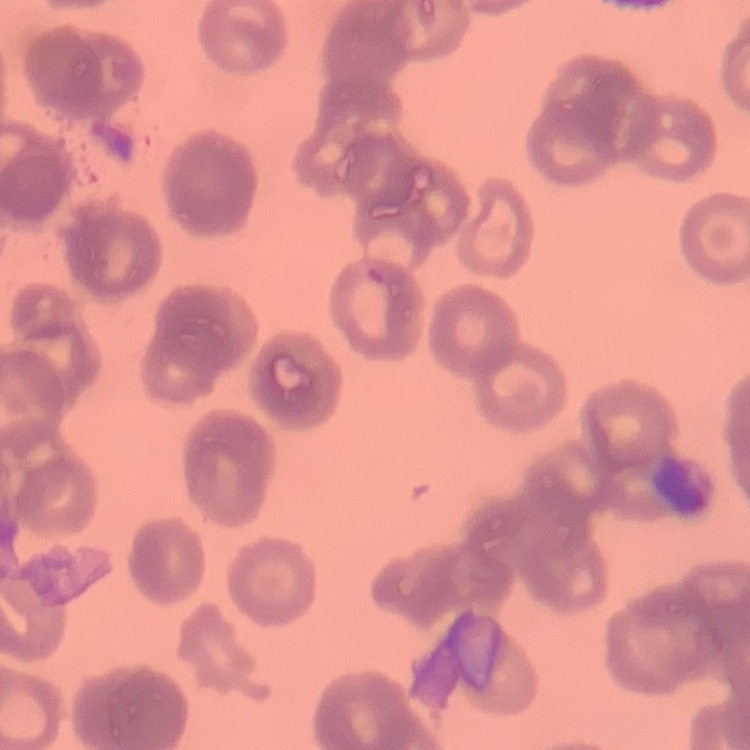 The red blood cells exhibit rouleaux formation. Square crop of a larger photomicrograph. Thin blood film. Stained with either Field's or Giemsa.